Name the parasite shown.
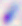
This is Toxoplasma gondii.

Micrograph. 400x magnification.